Classify this cell by malaria status.
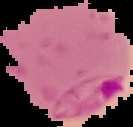

Parasitized.

Summary:
  - Image type: segmented cell region on a black background
  - Preparation: thin blood film
  - Image size: 133×127 pixels